Identify the blood parasite species.
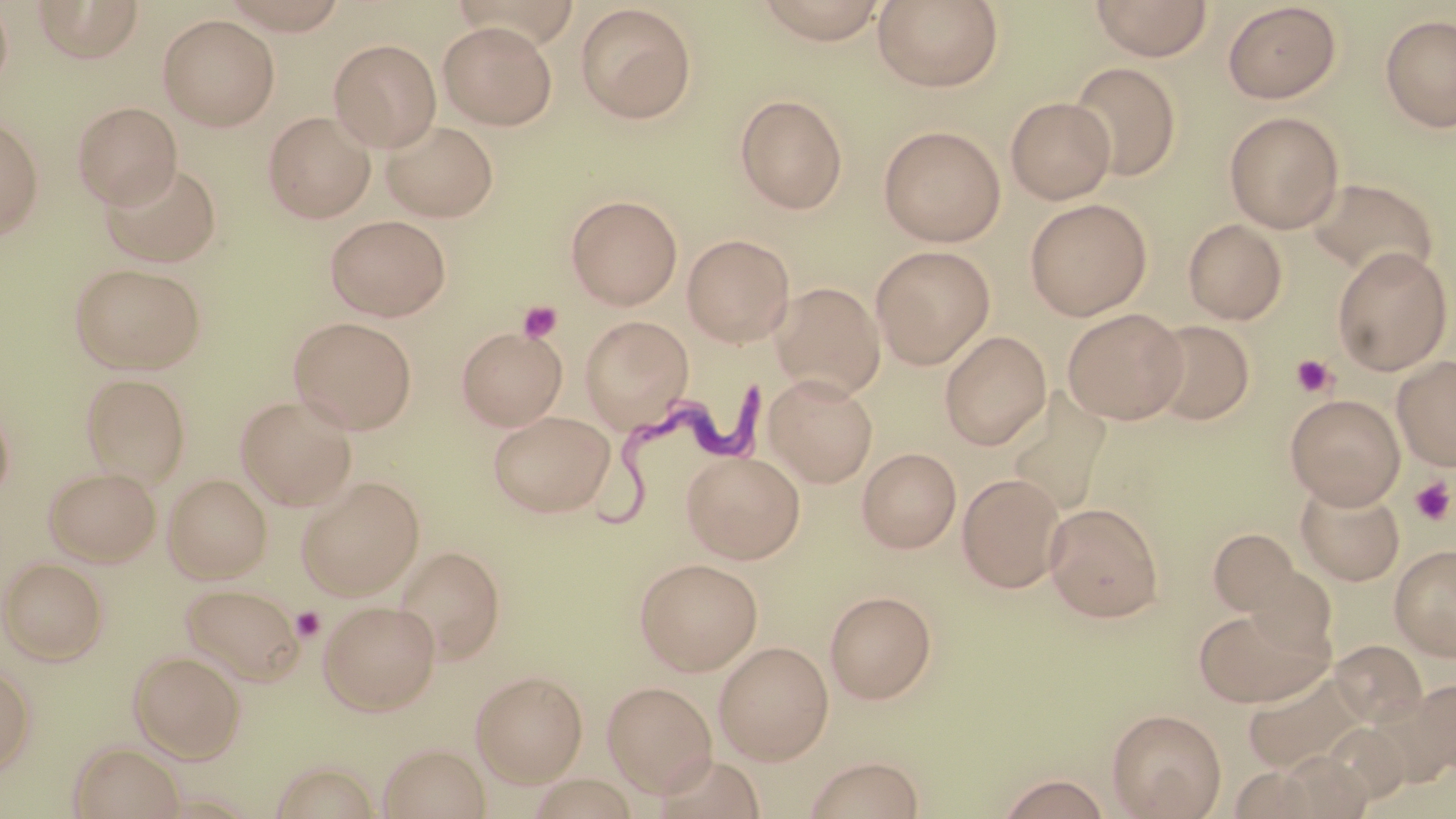

Trypanosoma brucei.

modality: light microscopy
trypanosoma_brucei_locations: 'approximate bounding boxes as [x1, y1, x2, y2] in pixels: [593, 372, 786, 540]'
uninfected_red_blood_cell_locations: 'approximate bounding boxes as [x1, y1, x2, y2] in pixels: [0, 0, 14, 93], [32, 0, 145, 64], [750, 0, 892, 45], [873, 0, 1005, 92], [1089, 0, 1214, 61], [213, 1, 356, 34], [1221, 2, 1342, 104], [574, 4, 697, 123], [158, 14, 280, 130], [1379, 14, 1456, 133], [438, 21, 558, 129], [329, 38, 441, 151], [1069, 61, 1182, 181], [736, 93, 848, 213], [1005, 96, 1116, 204], [72, 101, 182, 207], [263, 111, 376, 222], [1224, 111, 1344, 232], [0, 116, 44, 241], [381, 119, 499, 222], [878, 125, 1006, 246], [99, 159, 223, 268], [1305, 175, 1439, 279], [566, 194, 682, 309], [1024, 198, 1152, 320], [325, 214, 451, 321], [1183, 218, 1287, 324], [682, 233, 795, 346], [870, 245, 996, 368], [1331, 246, 1453, 374], [70, 262, 207, 373], [771, 281, 886, 399], [1062, 307, 1188, 423], [579, 315, 694, 431], [288, 316, 418, 433], [1146, 319, 1255, 424], [457, 326, 568, 430], [939, 331, 1052, 449], [1393, 355, 1456, 471], [81, 373, 190, 486], [764, 374, 878, 487], [1005, 392, 1111, 518], [1285, 394, 1405, 507], [0, 395, 15, 507], [235, 395, 357, 510], [487, 410, 615, 516], [857, 447, 961, 552], [681, 450, 805, 563], [43, 465, 161, 567], [163, 473, 273, 583], [958, 473, 1065, 591], [296, 476, 425, 599], [1296, 482, 1405, 586], [1045, 501, 1164, 622], [1206, 529, 1304, 617], [1390, 544, 1456, 661], [393, 545, 505, 663], [1, 557, 108, 664], [634, 557, 763, 675], [1242, 565, 1338, 657], [180, 582, 303, 683], [824, 590, 936, 703], [318, 599, 440, 715], [1194, 605, 1330, 708], [714, 640, 834, 764], [1328, 640, 1428, 726], [129, 650, 245, 761], [0, 662, 36, 777], [1244, 669, 1366, 772], [471, 670, 588, 786], [1411, 678, 1456, 775], [601, 680, 717, 796], [1107, 708, 1226, 818], [68, 741, 185, 819], [377, 742, 491, 819], [269, 756, 384, 818], [802, 756, 926, 818], [995, 772, 1114, 818]'
stain: May-Grünwald-Giemsa
field_of_view: single
image_size: 1456×819 pixels
platelet_locations: 'approximate bounding boxes as [x1, y1, x2, y2] in pixels: [517, 300, 563, 343], [1290, 354, 1338, 398], [1409, 476, 1455, 526], [291, 607, 325, 641]'
magnification: 1000x
preparation: thin blood smear